Locate every Plasmodium vivax-infected red blood cell.
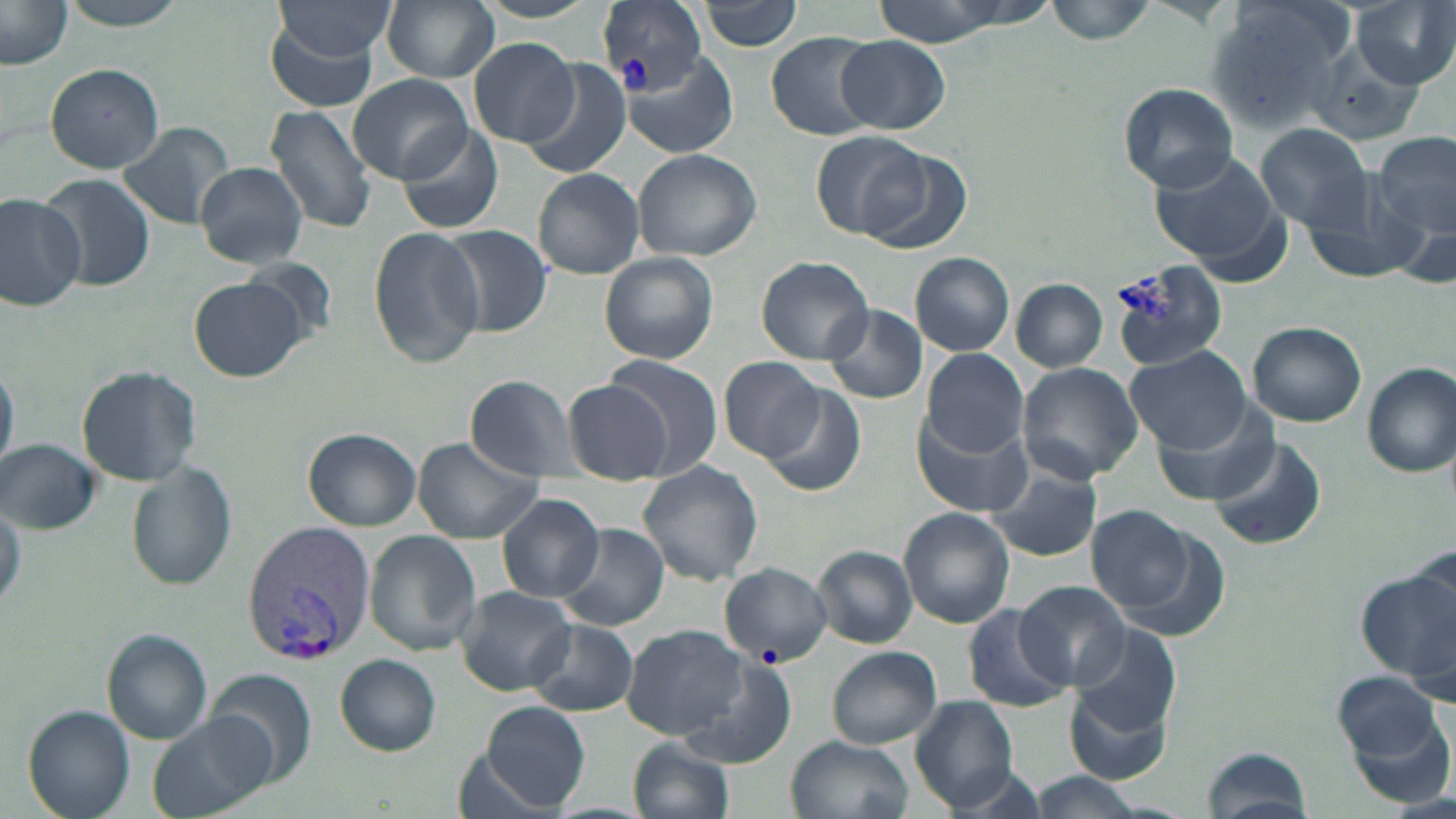
Approximate bounding boxes as named x1/y1/x2/y2 corners in pixels.
Plasmodium vivax-infected red blood cells: (x1=597, y1=2, x2=705, y2=102), (x1=241, y1=521, x2=375, y2=664).

Uninfected red blood cell locations: (x1=57, y1=0, x2=195, y2=29), (x1=382, y1=0, x2=499, y2=83), (x1=698, y1=0, x2=804, y2=52), (x1=862, y1=0, x2=1038, y2=43), (x1=1047, y1=0, x2=1157, y2=45), (x1=1206, y1=0, x2=1354, y2=130), (x1=1354, y1=0, x2=1455, y2=89), (x1=0, y1=2, x2=73, y2=69), (x1=274, y1=2, x2=398, y2=62), (x1=265, y1=16, x2=381, y2=114), (x1=766, y1=32, x2=879, y2=140), (x1=468, y1=37, x2=581, y2=147), (x1=836, y1=37, x2=950, y2=134), (x1=1309, y1=37, x2=1431, y2=145), (x1=622, y1=52, x2=734, y2=157), (x1=521, y1=62, x2=632, y2=182), (x1=44, y1=63, x2=167, y2=172), (x1=347, y1=72, x2=473, y2=185), (x1=1118, y1=82, x2=1240, y2=192), (x1=264, y1=105, x2=376, y2=233), (x1=116, y1=120, x2=237, y2=230), (x1=394, y1=121, x2=506, y2=237), (x1=1258, y1=124, x2=1374, y2=232), (x1=811, y1=130, x2=927, y2=240), (x1=1374, y1=131, x2=1455, y2=242), (x1=858, y1=147, x2=970, y2=253), (x1=631, y1=148, x2=762, y2=261), (x1=1150, y1=153, x2=1282, y2=267), (x1=195, y1=160, x2=308, y2=268), (x1=532, y1=169, x2=645, y2=279), (x1=42, y1=176, x2=154, y2=295), (x1=1302, y1=177, x2=1429, y2=287), (x1=0, y1=192, x2=87, y2=311), (x1=436, y1=225, x2=553, y2=337), (x1=369, y1=227, x2=485, y2=368), (x1=599, y1=252, x2=720, y2=364), (x1=910, y1=252, x2=1014, y2=356), (x1=756, y1=255, x2=875, y2=365), (x1=239, y1=257, x2=340, y2=349), (x1=1107, y1=259, x2=1228, y2=373), (x1=190, y1=277, x2=306, y2=380), (x1=1011, y1=278, x2=1107, y2=372), (x1=821, y1=304, x2=927, y2=405), (x1=1246, y1=321, x2=1368, y2=426), (x1=920, y1=346, x2=1028, y2=457), (x1=1126, y1=346, x2=1249, y2=452), (x1=597, y1=357, x2=723, y2=480), (x1=720, y1=357, x2=825, y2=461), (x1=0, y1=358, x2=18, y2=477), (x1=1020, y1=362, x2=1145, y2=484), (x1=1360, y1=363, x2=1455, y2=477), (x1=77, y1=364, x2=201, y2=486), (x1=464, y1=373, x2=582, y2=480), (x1=563, y1=380, x2=675, y2=483), (x1=757, y1=382, x2=868, y2=498), (x1=1152, y1=408, x2=1280, y2=506), (x1=913, y1=413, x2=1029, y2=517), (x1=303, y1=428, x2=422, y2=531), (x1=1208, y1=435, x2=1327, y2=550), (x1=412, y1=439, x2=543, y2=543), (x1=1, y1=440, x2=99, y2=534), (x1=636, y1=461, x2=766, y2=586), (x1=127, y1=462, x2=237, y2=589), (x1=986, y1=468, x2=1101, y2=560), (x1=498, y1=494, x2=605, y2=602), (x1=0, y1=501, x2=23, y2=617), (x1=900, y1=508, x2=1017, y2=629), (x1=1085, y1=508, x2=1203, y2=615), (x1=552, y1=522, x2=668, y2=633), (x1=364, y1=530, x2=482, y2=655), (x1=812, y1=547, x2=917, y2=649), (x1=721, y1=564, x2=832, y2=667), (x1=1359, y1=564, x2=1456, y2=685), (x1=1014, y1=582, x2=1132, y2=691), (x1=454, y1=586, x2=576, y2=694), (x1=960, y1=604, x2=1071, y2=713), (x1=525, y1=620, x2=637, y2=715), (x1=620, y1=624, x2=749, y2=741), (x1=1065, y1=626, x2=1183, y2=747), (x1=101, y1=629, x2=212, y2=744), (x1=827, y1=647, x2=941, y2=750), (x1=334, y1=653, x2=441, y2=757), (x1=684, y1=654, x2=796, y2=768), (x1=208, y1=667, x2=318, y2=789), (x1=1336, y1=673, x2=1454, y2=792), (x1=1066, y1=678, x2=1177, y2=787), (x1=910, y1=697, x2=1022, y2=811), (x1=481, y1=701, x2=590, y2=812), (x1=23, y1=705, x2=134, y2=818), (x1=149, y1=710, x2=275, y2=817), (x1=786, y1=736, x2=913, y2=819), (x1=627, y1=737, x2=734, y2=819), (x1=1202, y1=747, x2=1315, y2=817). Slide-level diagnosis: Plasmodium vivax. Image is 1456×819 pixels. 1000x magnification. Single field of view. Thin blood smear. May-Grünwald-Giemsa stain. Light microscopy.